Give the position of every Plasmodium parasite visible.
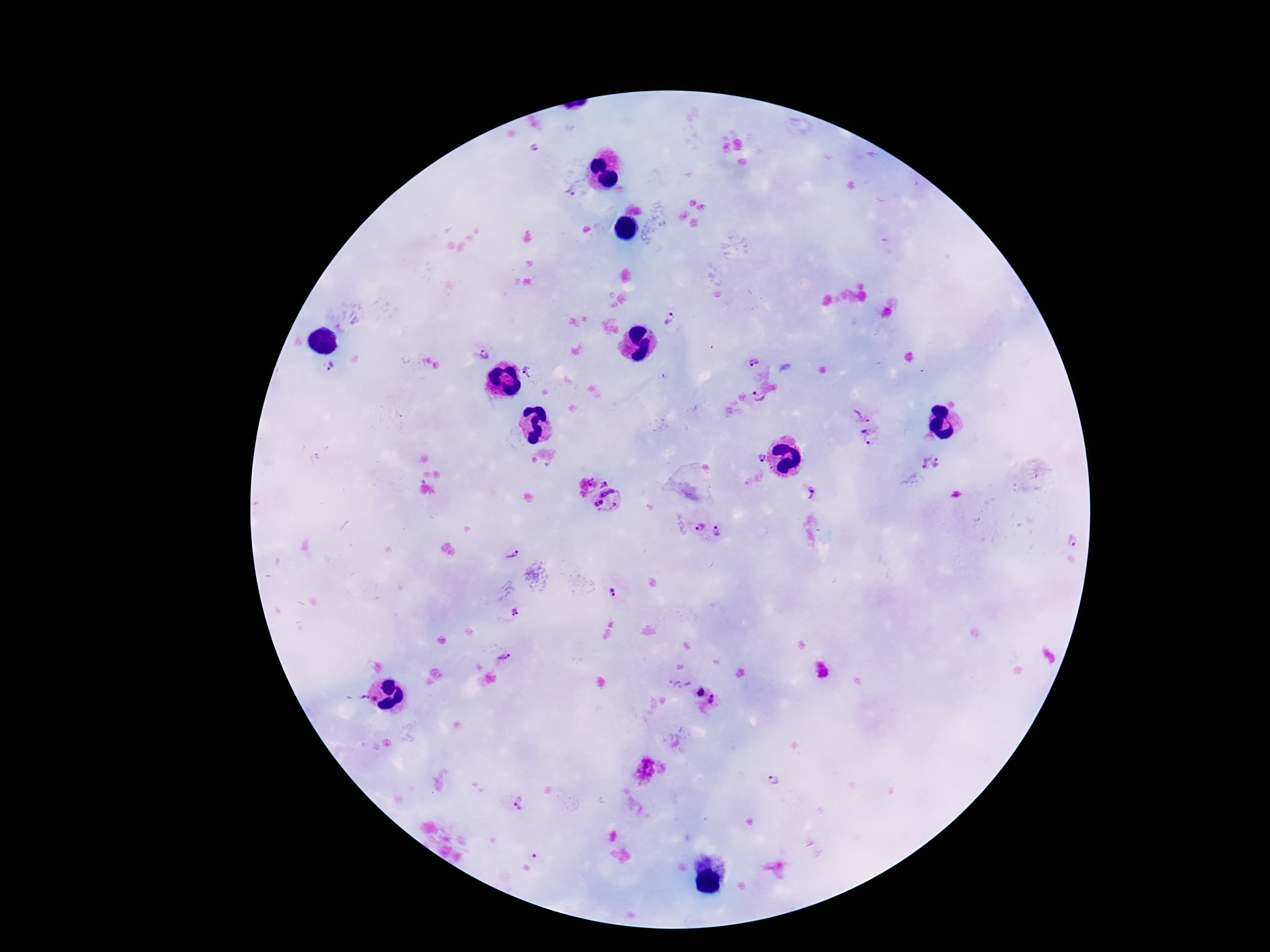
Approximate centers as {x, y} in pixels.
Plasmodium parasites: {535, 149}, {570, 190}, {671, 320}, {483, 355}, {752, 361}, {328, 367}, {529, 371}, {758, 397}, {863, 415}, {868, 438}, {760, 460}, {930, 463}, {605, 479}, {813, 493}, {608, 503}, {700, 529}, {718, 532}, {1070, 543}, {510, 553}, {611, 590}, {515, 613}, {505, 658}, {699, 693}, {716, 701}, {773, 781}, {519, 804}, {534, 857}.

Photographed through the microscope eyepiece with a smartphone camera. Image is 1270×952 pixels. Giemsa-stained preparation. 100x magnification. Thick blood film. Single field of view. Patient malaria status: positive.